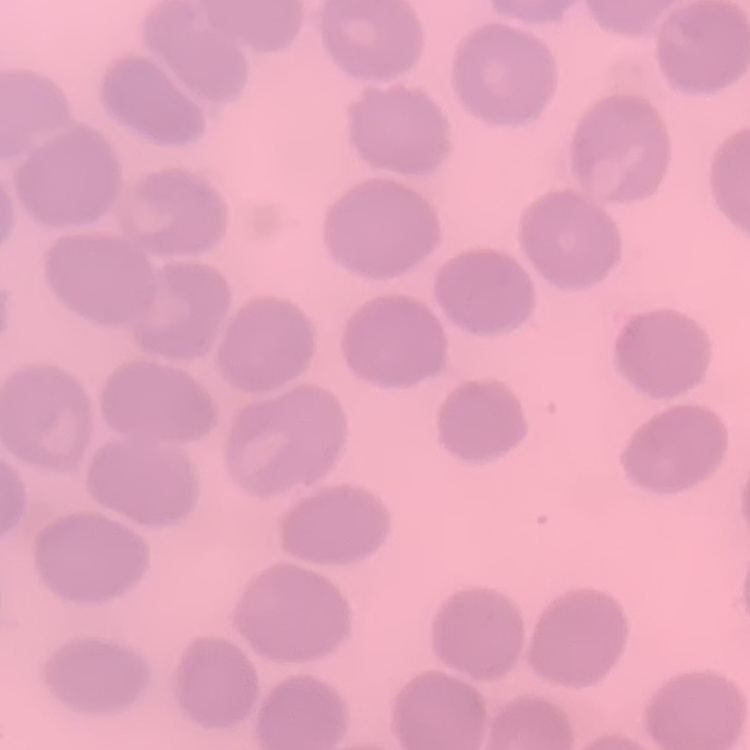

The red blood cells show no rouleaux formation. Thin blood smear. Field's or Giemsa stain. Square crop of a larger photomicrograph.